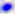
modality = photomicrograph
identification = Toxoplasma gondii
magnification = 400x